Give the position of every Plasmodium parasite visible.
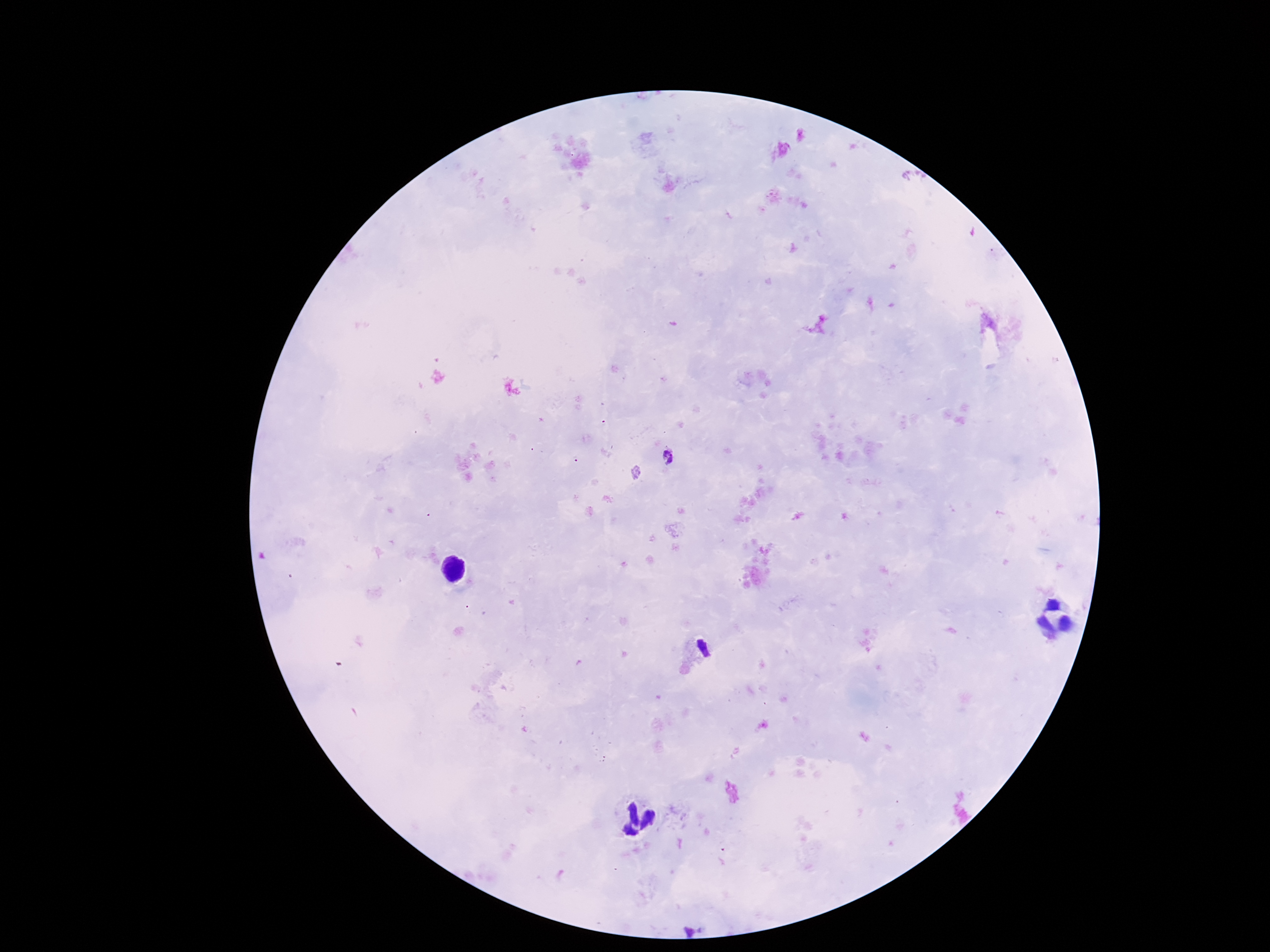

Approximate centers as {x, y} in pixels.
Plasmodium parasites: {667, 457}.

field of view = one from this slide
patient malaria status = infected
image size = 1270×952 pixels
preparation = thick blood smear
capture = smartphone camera through the microscope eyepiece
magnification = 100x
stain = Giemsa